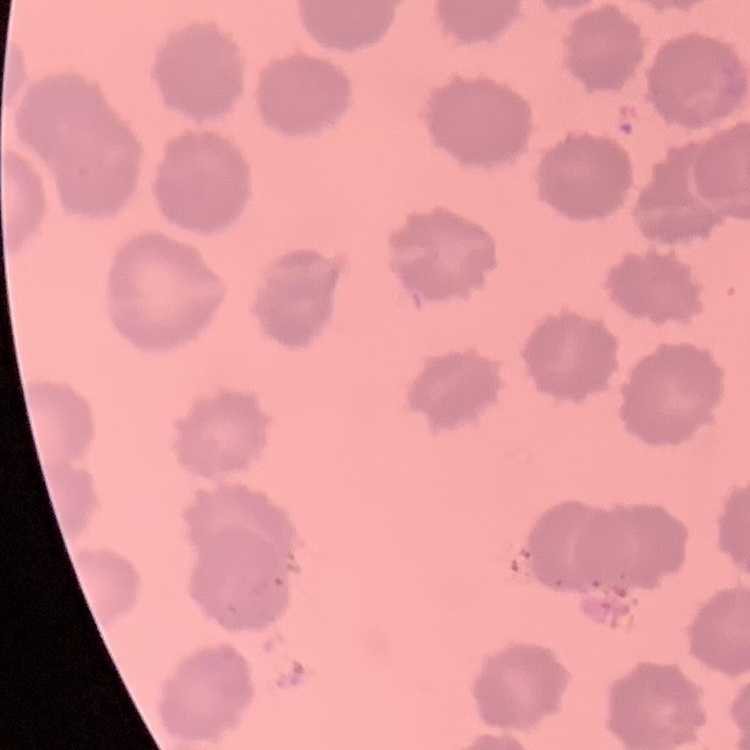 The erythrocytes show no rouleaux formation. Stained with either Field's or Giemsa. Square crop of a larger photomicrograph. Thin blood smear.